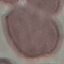
Result: no malaria parasites seen. Photographed with a smartphone camera at the microscope eyepiece. Giemsa stain. Thin smear of blood. Cell patch, automatically extracted from a larger field of view and resized to 64 × 64 pixels.